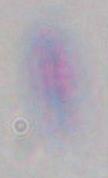
Summary:
  - Magnification: 1000x
  - Identification: Toxoplasma gondii
  - Modality: photomicrograph